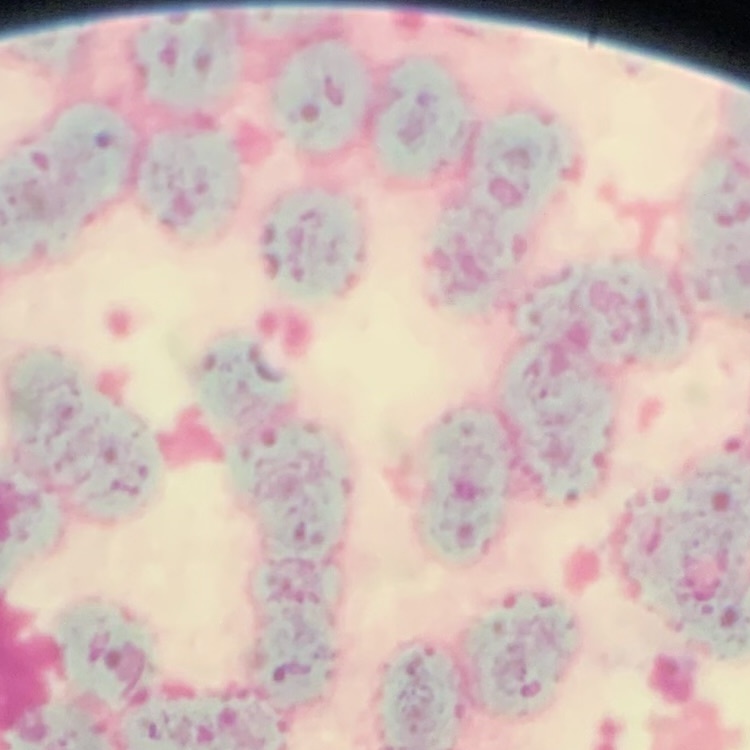 The red blood cells show rouleaux formation. Thin blood film. Square crop of a larger photomicrograph. Field's or Giemsa stain.